State which parasite is depicted.
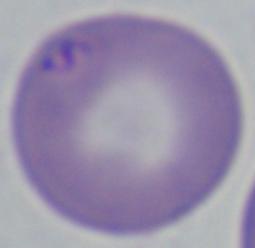

This is Babesia.

magnification: 1000x
modality: photomicrograph